Report the malaria status of this cell.
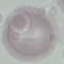

Uninfected.

Summary:
  - Image type: automatically extracted cell patch, resized to 64 × 64 pixels
  - Preparation: thin blood smear
  - Capture: smartphone camera at the microscope eyepiece
  - Stain: Giemsa